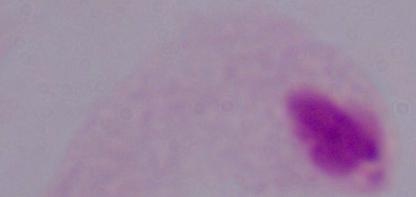

magnification = 1000x
modality = photomicrograph
identification = trichomonad